State the blood parasite species.
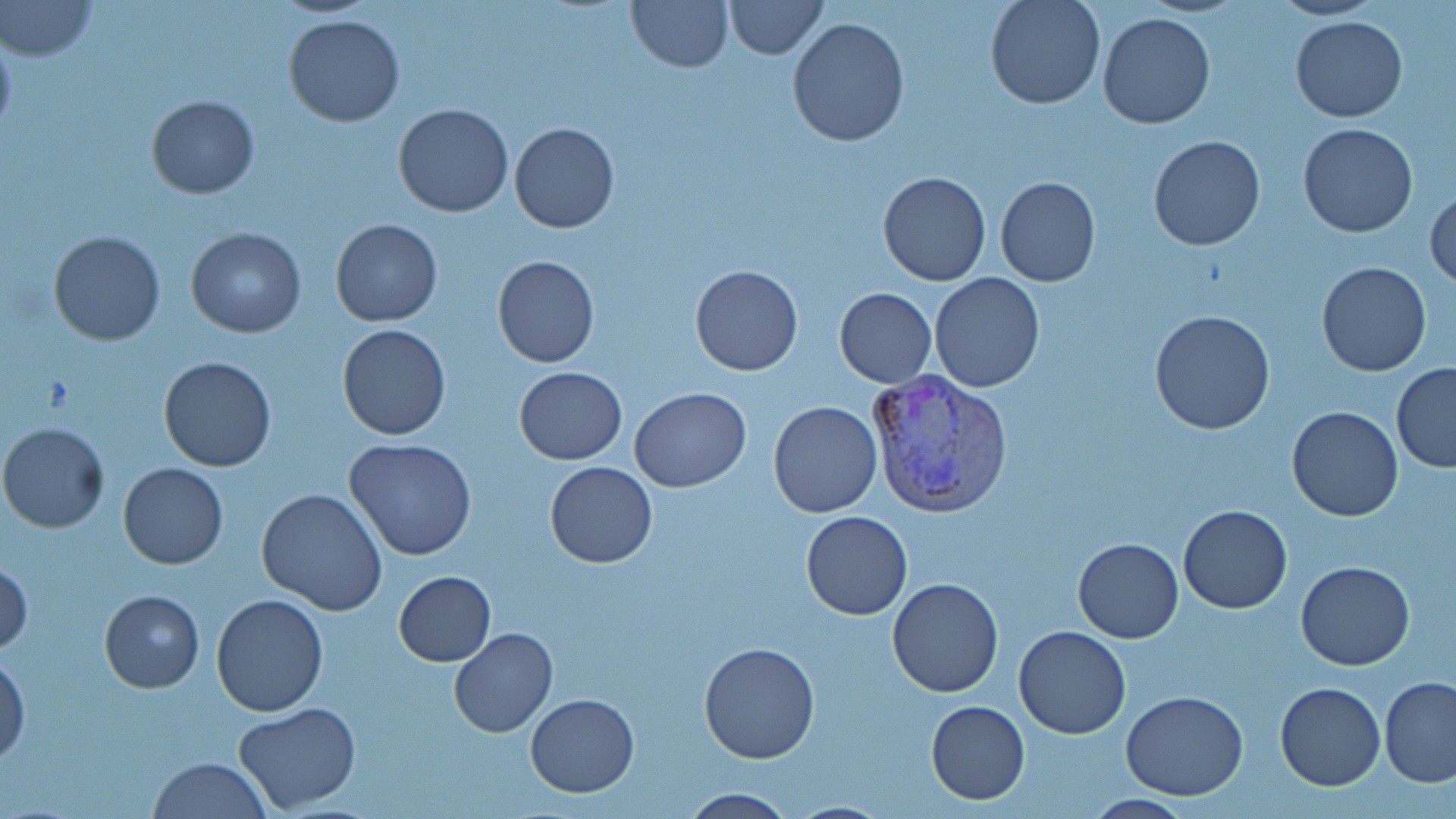
Plasmodium vivax.

magnification = 1000x
stain = May-Grünwald-Giemsa
field of view = one of a larger specimen
image size = 1456×819 pixels
modality = light microscopy
preparation = thin blood film
Plasmodium vivax-infected red blood cell locations = approximate bounding boxes as (x1, y1, x2, y2) in pixels: (866, 368, 1014, 517)
uninfected red blood cell locations = approximate bounding boxes as (x1, y1, x2, y2) in pixels: (1, 0, 97, 61), (627, 0, 734, 72), (724, 0, 828, 59), (984, 0, 1105, 110), (1269, 0, 1384, 20), (1099, 11, 1217, 128), (283, 15, 406, 128), (1291, 16, 1407, 122), (787, 18, 911, 148), (0, 30, 17, 138), (146, 96, 260, 199), (393, 102, 515, 217), (1298, 121, 1418, 237), (509, 122, 620, 233), (1150, 136, 1265, 251), (877, 171, 991, 287), (995, 177, 1101, 288), (1425, 186, 1456, 291), (330, 218, 443, 327), (187, 227, 307, 337), (49, 230, 165, 345), (493, 256, 598, 369), (1317, 261, 1432, 377), (691, 264, 803, 376), (930, 272, 1046, 392), (834, 287, 937, 387), (1149, 309, 1277, 435), (338, 323, 450, 440), (158, 355, 277, 472), (1393, 364, 1456, 471), (514, 366, 627, 464), (629, 388, 750, 492), (768, 401, 883, 517), (1287, 405, 1403, 522), (0, 422, 110, 533), (344, 437, 477, 560), (544, 461, 657, 568), (118, 462, 228, 569), (257, 487, 387, 615), (1178, 503, 1292, 614), (801, 511, 913, 620), (1071, 538, 1183, 641), (0, 560, 33, 655), (1296, 561, 1415, 670), (393, 571, 495, 666), (886, 577, 1003, 697), (99, 589, 204, 692), (211, 594, 328, 716), (1014, 624, 1131, 740), (449, 628, 558, 738), (698, 642, 820, 764), (1, 654, 29, 764), (1379, 676, 1455, 787), (1275, 681, 1385, 791), (1121, 690, 1250, 800), (525, 693, 639, 797), (927, 700, 1031, 804), (233, 702, 362, 814), (148, 757, 272, 818), (678, 789, 799, 817), (783, 800, 896, 817)